Report the malaria status of this cell.
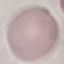

Uninfected.

Giemsa-stained preparation. Acquired by smartphone through the microscope eyepiece. Cell patch, automatically extracted from a larger field of view and resized to 64 × 64 pixels. Thin blood film.